Name the parasite shown.
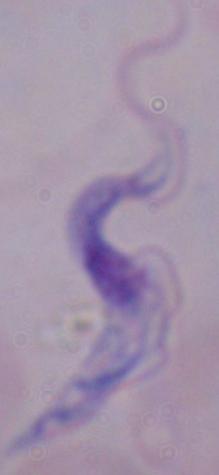

A trypanosome.

Summary:
  - Magnification: 1000x
  - Modality: micrograph